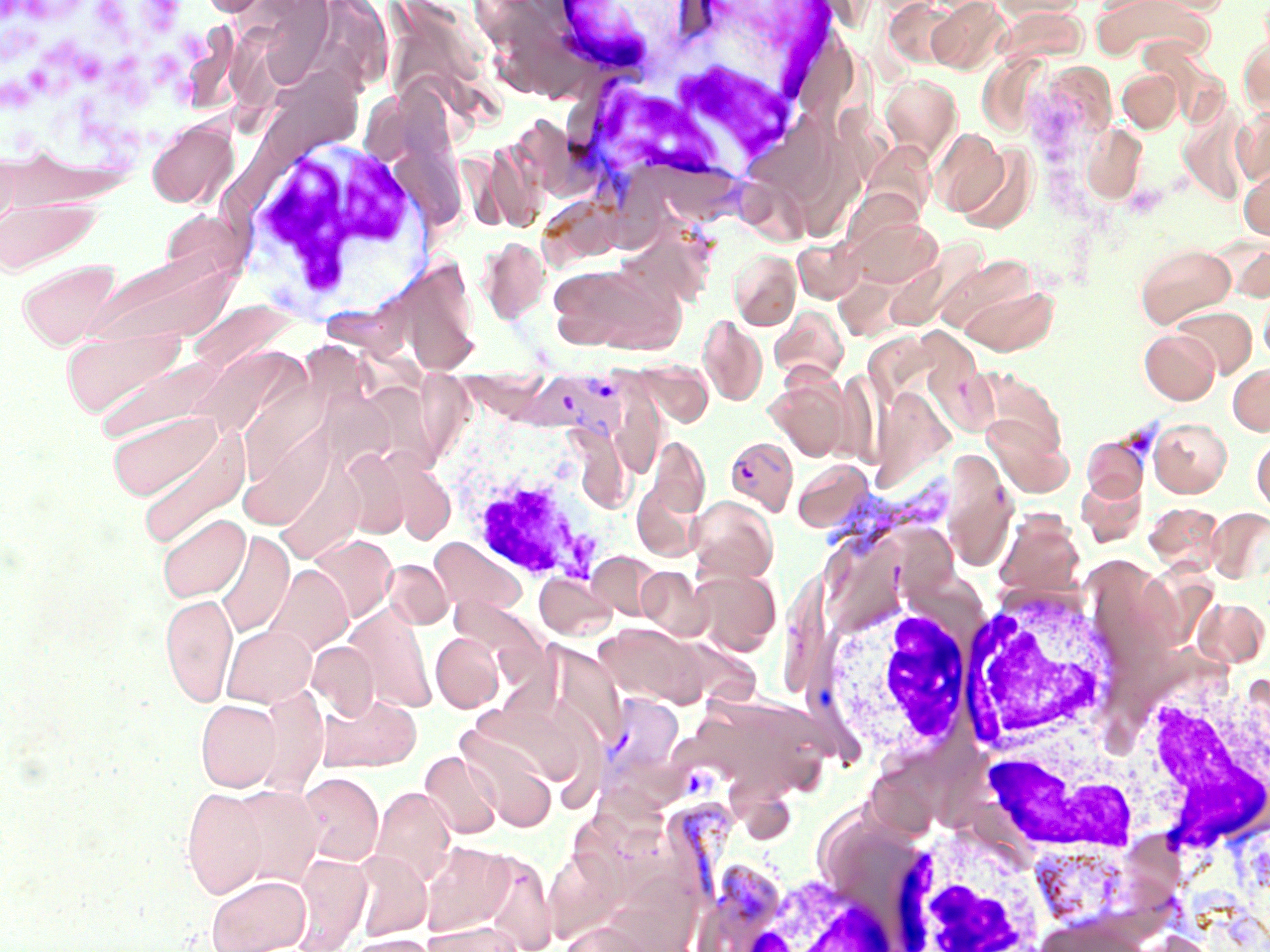 Approximate bounding boxes as [x1, y1, x2, y2] in pixels. Platelet locations: [0, 0, 64, 31], [91, 0, 134, 37], [143, 0, 188, 36], [178, 28, 209, 66], [44, 32, 109, 89], [113, 47, 145, 89], [150, 52, 188, 91], [0, 76, 40, 111]. White blood cell locations: [545, 1, 686, 77], [555, 9, 834, 214], [230, 132, 431, 319], [442, 422, 623, 588], [957, 580, 1125, 759], [814, 594, 977, 768], [1137, 669, 1270, 865], [968, 729, 1161, 860], [882, 821, 1052, 951], [685, 842, 910, 952]. Uninfected red blood cell locations: [927, 0, 1011, 75], [990, 0, 1088, 21], [1092, 0, 1215, 64], [1143, 0, 1230, 15], [261, 1, 339, 93], [1238, 35, 1270, 119], [267, 67, 360, 167], [1117, 69, 1181, 133], [879, 74, 962, 163], [1232, 106, 1270, 188], [146, 118, 239, 209], [1080, 122, 1147, 205], [929, 127, 1010, 218], [864, 140, 942, 227], [952, 141, 1038, 234], [397, 146, 466, 234], [1239, 166, 1270, 241], [0, 195, 102, 276], [844, 213, 942, 289], [478, 236, 551, 324], [792, 236, 865, 303], [1134, 242, 1235, 327], [80, 247, 245, 351], [729, 249, 801, 330], [367, 253, 483, 375], [17, 258, 121, 351], [546, 261, 686, 354], [949, 275, 1061, 355], [1259, 288, 1270, 364], [769, 305, 848, 383], [1172, 305, 1257, 378], [698, 314, 767, 406], [61, 324, 186, 418], [1139, 329, 1219, 404], [189, 351, 295, 431], [89, 352, 222, 443], [638, 360, 712, 426], [1228, 362, 1270, 435], [766, 374, 853, 460], [870, 393, 954, 493], [980, 400, 1070, 495], [237, 403, 336, 535], [106, 409, 227, 506], [1149, 417, 1231, 497], [133, 418, 250, 547], [645, 435, 710, 521], [1081, 435, 1149, 502], [1251, 435, 1270, 515], [329, 444, 405, 626], [339, 447, 412, 538], [792, 459, 874, 533], [1076, 474, 1146, 544], [687, 495, 778, 583], [1143, 503, 1224, 573], [1206, 507, 1270, 583], [995, 510, 1085, 597], [158, 512, 250, 602], [215, 529, 294, 638], [308, 535, 397, 624], [428, 537, 525, 617], [586, 551, 663, 621], [384, 559, 453, 629], [263, 563, 352, 656], [636, 566, 711, 639], [689, 568, 781, 656], [536, 572, 616, 640], [160, 592, 238, 706], [1191, 597, 1269, 668], [343, 606, 436, 713], [597, 623, 712, 703], [222, 624, 316, 708], [431, 632, 504, 713], [307, 641, 380, 720], [252, 686, 329, 797], [316, 693, 421, 772], [195, 699, 282, 792], [472, 701, 581, 786], [457, 725, 558, 830], [419, 750, 503, 839], [297, 772, 383, 867], [181, 785, 268, 899], [228, 785, 325, 888], [369, 786, 456, 887], [419, 841, 516, 938], [543, 843, 630, 941], [460, 847, 558, 952], [351, 851, 432, 940], [290, 853, 372, 952], [206, 874, 310, 952], [1035, 915, 1149, 952], [422, 920, 527, 951], [559, 920, 657, 952], [342, 933, 441, 952]. Plasmodium vivax-infected red blood cell locations: [525, 370, 633, 445], [725, 436, 798, 515], [597, 691, 685, 783]. Slide-level diagnosis: Plasmodium vivax. Single field of view. Thin blood film. Image is 1270×952 pixels. May-Grünwald-Giemsa-stained preparation. 1000x magnification. Light microscopy.